Classify this cell by malaria status.
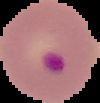

It is parasitized.

{
  "image_type": "cell region segmented out of the field of view; surrounding area masked to black",
  "preparation": "thin blood smear",
  "image_size": "100×103 pixels"
}